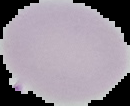
Summary:
  - Result: no Plasmodium parasites seen
  - Preparation: thin blood smear
  - Image type: segmented cell region with the area outside set to black
  - Image size: 130×106 pixels